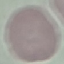

malaria status = uninfected
preparation = thin smear
image type = automatically extracted cell patch, resized to 64 × 64 pixels
capture = smartphone through the microscope eyepiece
stain = Giemsa